Point out every malaria parasite.
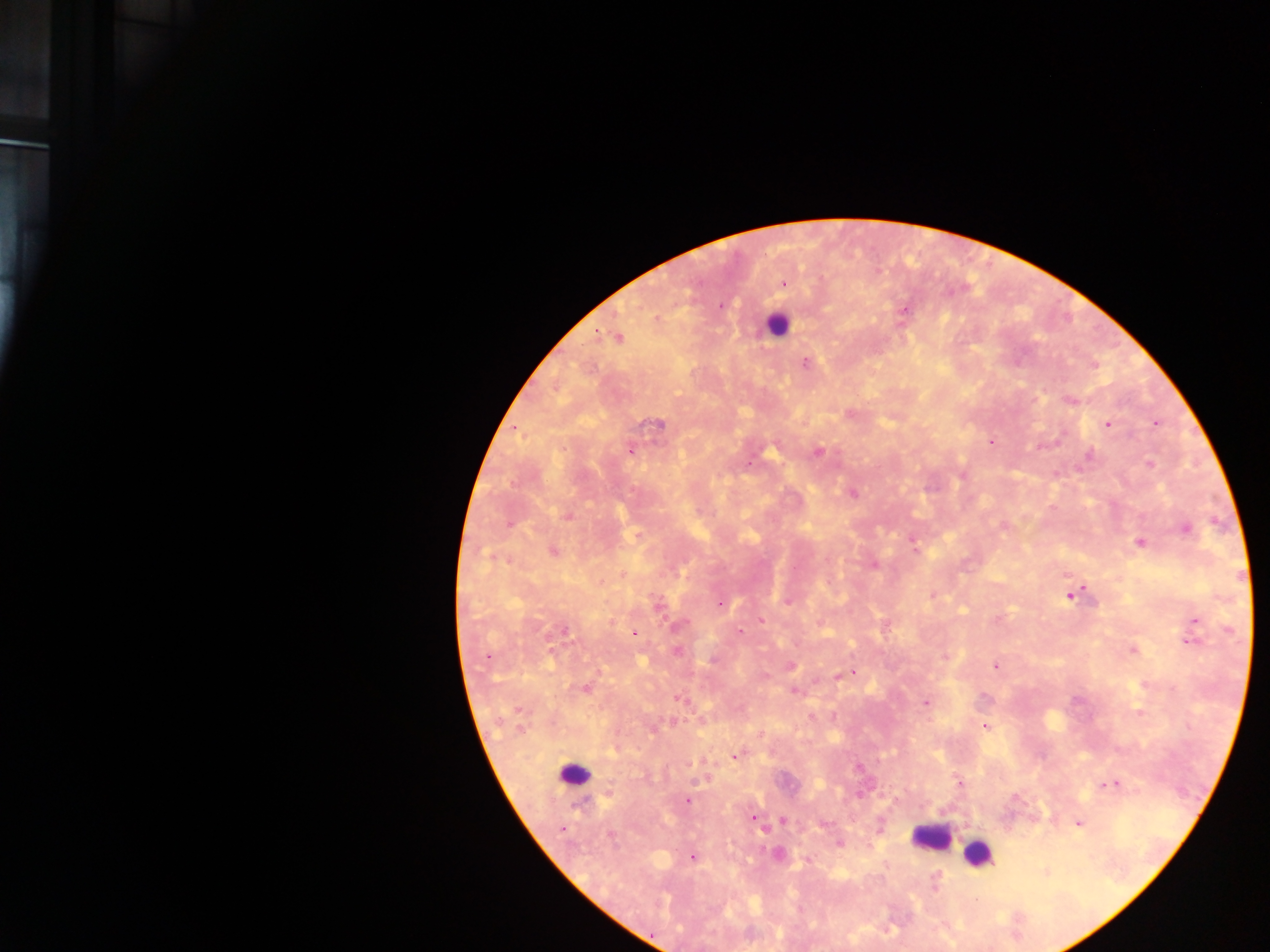
Approximate centers as x y in pixels.
Malaria parasites: 784 284; 721 306; 904 310; 596 334; 618 337; 806 363; 1070 400; 850 413; 1155 422; 657 423; 1107 424; 991 442; 630 450; 817 452; 1090 456; 1150 464; 962 475; 853 493; 568 515; 509 525; 1003 525; 1187 529; 913 541; 1139 543; 914 547; 553 552; 489 556; 874 565; 1071 595; 932 596; 787 602; 721 603; 657 605; 761 620; 1195 621; 678 625; 565 631; 634 632; 740 632; 1191 641; 677 650; 1133 650; 551 651; 487 657; 944 657; 714 660; 791 666; 995 666; 853 673; 846 674; 764 676; 839 676; 585 689; 794 691; 678 698; 926 703; 519 710; 1139 713; 811 717; 672 722; 985 726; 520 730; 760 734; 737 756; 959 783; 1111 784; 688 801; 754 817; 783 820; 1078 824; 562 829; 611 835; 778 853; 692 858; 936 882.

Summary:
  - Leukocyte locations: 775 325; 574 775; 930 837; 978 853
  - Capture: mobile-phone photograph through a microscope
  - Image size: 1270×952 pixels
  - Country: Ghana
  - Field of view: single
  - Preparation: thick blood film